Locate every blood parasite and identify its species.
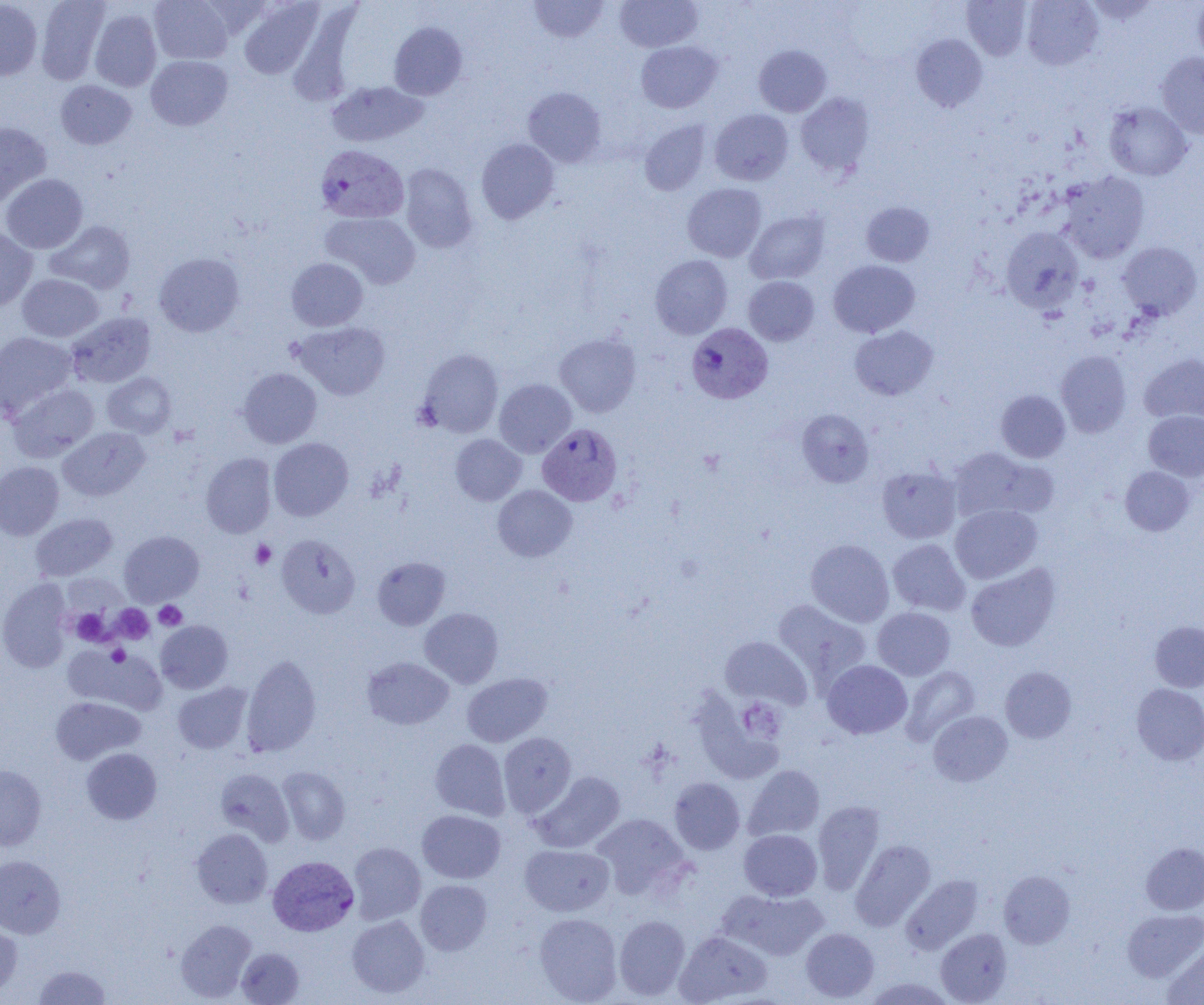

Approximate bounding boxes as [x1, y1, x2, y2] in pixels.
Plasmodium vivax-infected red blood cells: [316, 144, 410, 224], [687, 322, 773, 404], [537, 423, 622, 506], [268, 855, 359, 936].
No Plasmodium falciparum, Plasmodium ovale, Plasmodium malariae, Babesia divergens, or Trypanosoma brucei observed.

Platelet locations: [250, 540, 276, 569], [153, 601, 186, 630], [113, 605, 154, 643], [69, 608, 111, 645], [106, 645, 128, 666], [739, 699, 786, 743]. Uninfected red blood cell locations: [0, 0, 42, 80], [36, 0, 111, 84], [149, 0, 233, 64], [529, 0, 608, 43], [615, 0, 702, 52], [962, 0, 1031, 60], [1022, 0, 1103, 70], [1193, 0, 1204, 65], [238, 1, 324, 79], [1085, 1, 1161, 24], [90, 9, 162, 91], [389, 22, 467, 100], [911, 34, 987, 112], [635, 41, 722, 113], [753, 45, 831, 117], [1156, 53, 1204, 139], [146, 55, 233, 131], [55, 80, 136, 150], [326, 81, 428, 148], [522, 87, 606, 167], [796, 92, 875, 177], [1104, 102, 1192, 180], [710, 109, 793, 185], [638, 120, 712, 195], [0, 122, 51, 207], [476, 138, 559, 224], [399, 163, 477, 253], [1059, 171, 1149, 263], [1, 174, 88, 253], [682, 183, 767, 262], [861, 202, 934, 267], [745, 210, 830, 284], [322, 212, 421, 289], [45, 220, 136, 294], [0, 226, 38, 311], [1001, 226, 1084, 314], [1117, 241, 1202, 320], [154, 253, 244, 337], [650, 255, 733, 339], [286, 258, 368, 331], [828, 260, 920, 337], [17, 274, 104, 342], [743, 276, 818, 345], [66, 312, 156, 388], [293, 321, 390, 400], [850, 325, 938, 400], [0, 331, 78, 420], [554, 333, 641, 417], [417, 348, 504, 437], [1056, 350, 1131, 437], [1140, 353, 1204, 424], [238, 367, 322, 448], [102, 372, 176, 437], [494, 379, 576, 457], [8, 383, 99, 462], [996, 390, 1070, 462], [797, 408, 873, 488], [1144, 410, 1204, 481], [58, 427, 150, 501], [450, 434, 526, 505], [269, 438, 353, 521], [949, 447, 1056, 524], [201, 453, 276, 538], [0, 461, 64, 539], [877, 465, 961, 543], [1120, 466, 1194, 535], [493, 484, 577, 562], [950, 504, 1042, 583], [30, 512, 117, 581], [119, 531, 204, 606], [277, 534, 360, 618], [805, 539, 894, 627], [887, 539, 970, 616], [373, 557, 450, 630], [965, 563, 1060, 652], [0, 579, 73, 671], [773, 599, 871, 688], [873, 607, 955, 680], [419, 608, 503, 688], [155, 620, 233, 693], [1149, 621, 1204, 692], [720, 636, 812, 709], [63, 645, 167, 715], [241, 655, 321, 757], [362, 657, 453, 729], [822, 660, 912, 739], [900, 666, 980, 745], [1000, 667, 1076, 743], [462, 672, 552, 747], [172, 683, 251, 753], [1132, 683, 1204, 765], [689, 690, 784, 782], [51, 696, 145, 764], [928, 710, 1012, 786], [498, 732, 576, 816], [430, 739, 510, 819], [82, 748, 161, 824], [0, 765, 47, 850], [743, 765, 824, 841], [277, 766, 351, 845], [215, 768, 293, 845], [531, 772, 625, 853], [669, 777, 745, 855], [813, 801, 885, 893], [417, 810, 505, 883], [591, 813, 691, 899], [191, 828, 273, 908], [739, 829, 822, 900], [850, 840, 935, 930], [348, 842, 426, 924], [1141, 843, 1204, 914], [520, 844, 614, 916], [0, 855, 65, 938], [999, 871, 1075, 948], [902, 875, 983, 954], [415, 879, 492, 955], [719, 889, 827, 960], [1123, 909, 1204, 981], [534, 913, 622, 1004], [347, 915, 429, 998], [614, 915, 690, 999], [175, 919, 256, 1002], [0, 921, 23, 997], [801, 928, 879, 1002], [936, 928, 1012, 1004], [675, 931, 771, 1004], [1162, 944, 1204, 1005], [236, 947, 304, 1004], [33, 964, 111, 1004], [862, 977, 957, 1005]. Slide-level diagnosis: Plasmodium vivax. 1000x magnification. Image is 1204×1005 pixels. Single field of view. Optical microscopy. Thin blood smear.